Identify the parasite.
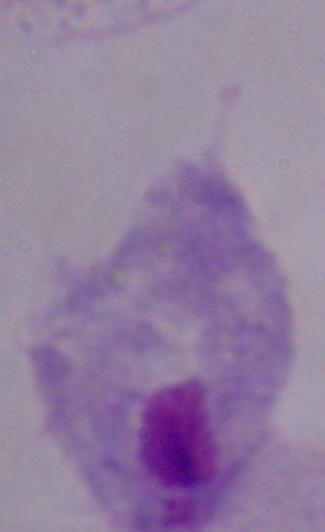
A trichomonad.

Micrograph. 1000x magnification.